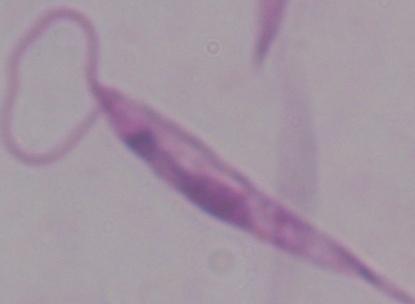 Photomicrograph. A Leishmania parasite is shown. 1000x magnification.